Outline each uninfected red blood cell.
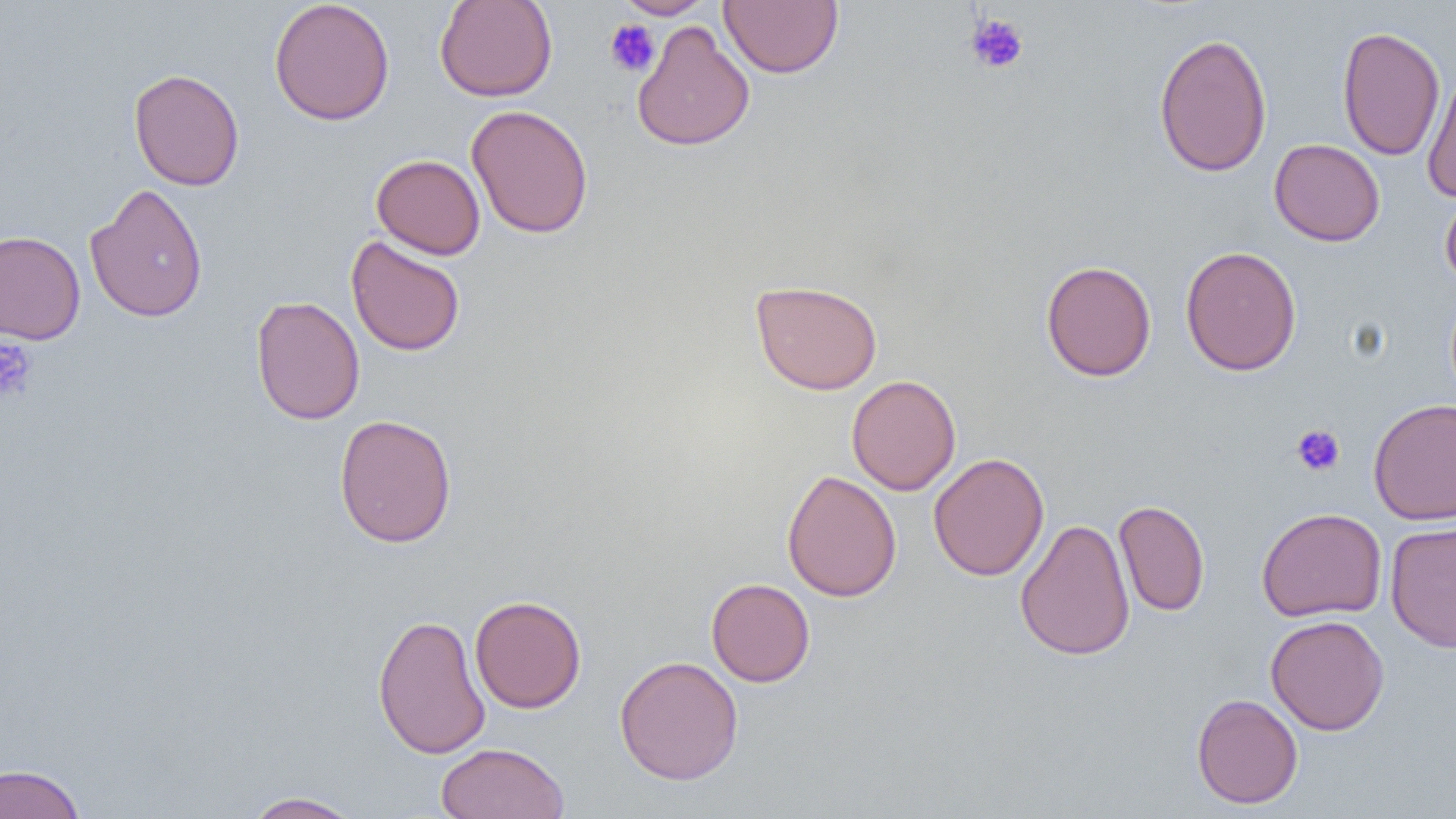
Approximate bounding boxes as named x1/y1/x2/y2 corners in pixels.
Uninfected red blood cells: (x1=268, y1=0, x2=396, y2=126), (x1=434, y1=0, x2=558, y2=102), (x1=616, y1=0, x2=715, y2=19), (x1=719, y1=1, x2=843, y2=78), (x1=631, y1=21, x2=755, y2=152), (x1=1337, y1=25, x2=1446, y2=161), (x1=1153, y1=32, x2=1272, y2=178), (x1=1423, y1=67, x2=1456, y2=202), (x1=129, y1=68, x2=244, y2=190), (x1=466, y1=104, x2=594, y2=239), (x1=1269, y1=139, x2=1385, y2=246), (x1=371, y1=154, x2=485, y2=259), (x1=85, y1=183, x2=209, y2=323), (x1=1440, y1=187, x2=1456, y2=290), (x1=0, y1=230, x2=85, y2=344), (x1=346, y1=235, x2=465, y2=357), (x1=1180, y1=245, x2=1302, y2=376), (x1=1041, y1=260, x2=1156, y2=381), (x1=750, y1=279, x2=883, y2=395), (x1=250, y1=295, x2=365, y2=425), (x1=846, y1=374, x2=961, y2=496), (x1=1368, y1=398, x2=1456, y2=525), (x1=333, y1=413, x2=457, y2=548), (x1=928, y1=452, x2=1049, y2=581), (x1=782, y1=469, x2=901, y2=603), (x1=1113, y1=500, x2=1210, y2=616), (x1=1256, y1=507, x2=1387, y2=622), (x1=1015, y1=518, x2=1135, y2=661), (x1=1385, y1=521, x2=1456, y2=653), (x1=706, y1=578, x2=815, y2=687), (x1=469, y1=594, x2=586, y2=713), (x1=372, y1=613, x2=490, y2=760), (x1=1265, y1=614, x2=1390, y2=735), (x1=614, y1=655, x2=744, y2=785), (x1=1191, y1=693, x2=1303, y2=809), (x1=435, y1=742, x2=570, y2=819), (x1=0, y1=763, x2=87, y2=819), (x1=241, y1=791, x2=365, y2=819).

slide_level_diagnosis: no evidence of blood parasites
preparation: thin blood smear
modality: optical microscopy
magnification: 1000x
platelet_locations: 'approximate bounding boxes as named x1/y1/x2/y2 corners in pixels: (x1=965, y1=13, x2=1030, y2=75), (x1=605, y1=18, x2=660, y2=78), (x1=0, y1=337, x2=37, y2=403), (x1=1291, y1=424, x2=1346, y2=477)'
field_of_view: one of a larger specimen
image_size: 1456×819 pixels